Report the malaria status of this cell.
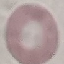
Uninfected.

Summary:
  - Image type: cell patch, automatically extracted from a larger field of view and resized to 64 × 64 pixels
  - Preparation: thin smear
  - Stain: Giemsa
  - Capture: smartphone camera at the microscope eyepiece